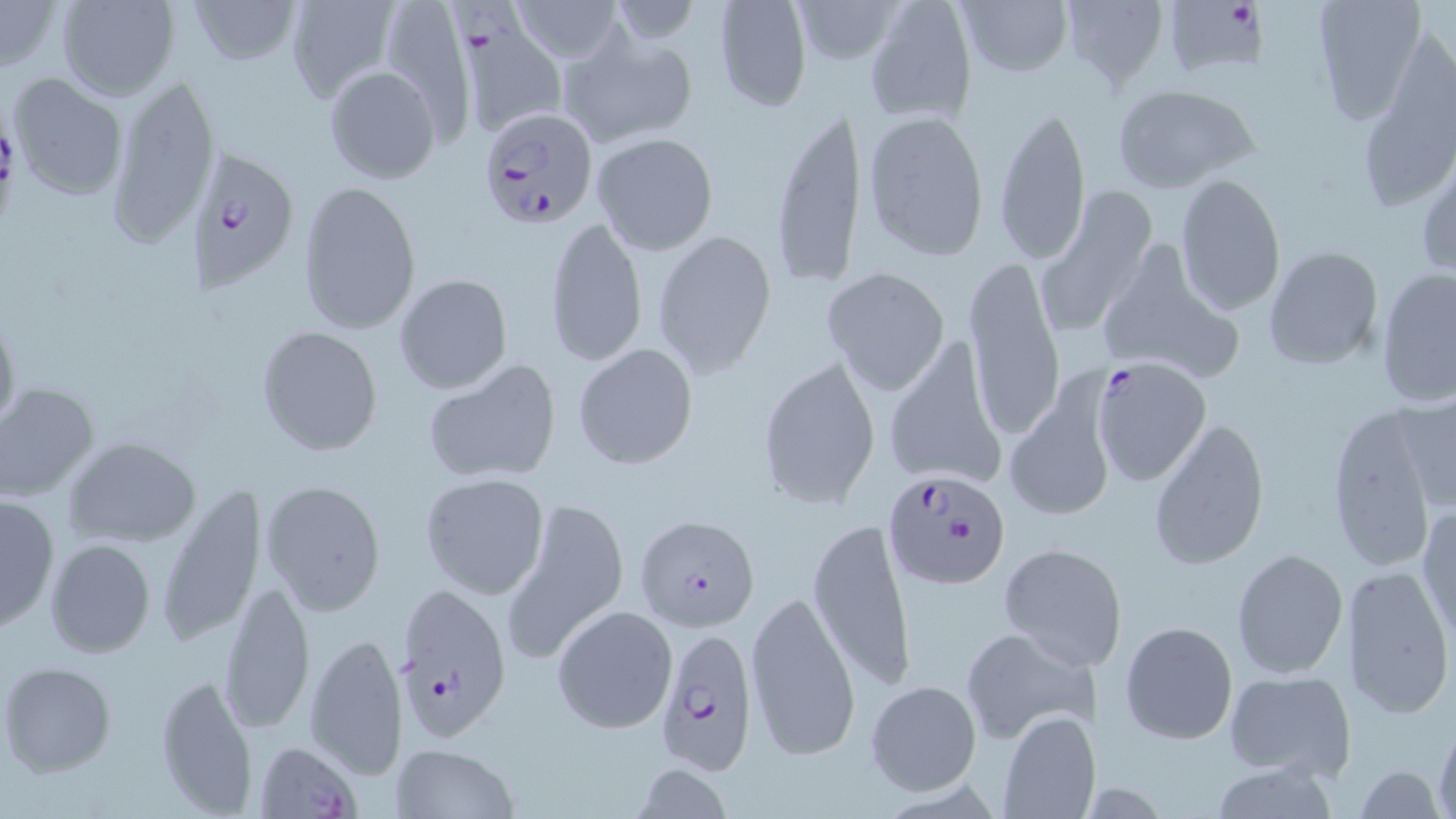

slide_level_diagnosis: Plasmodium falciparum
magnification: 1000x
uninfected_red_blood_cell_locations: 'approximate bounding boxes as (x1,y1)-(x2,y2) corner pairs in pixels: (0,0)-(60,73), (58,0)-(181,102), (184,0)-(304,69), (792,0)-(903,67), (864,0)-(978,125), (954,0)-(1075,79), (1055,0)-(1172,92), (1310,0)-(1428,121), (285,1)-(399,103), (514,1)-(621,62), (712,1)-(813,112), (557,25)-(697,147), (324,63)-(443,184), (6,73)-(128,202), (105,73)-(222,247), (1113,84)-(1258,192), (994,101)-(1091,269), (770,105)-(865,291), (863,108)-(990,262), (591,132)-(719,256), (1417,157)-(1455,279), (1173,173)-(1287,317), (298,180)-(421,335), (1039,183)-(1159,331), (543,214)-(646,370), (652,228)-(777,375), (1095,242)-(1242,381), (1264,245)-(1384,370), (961,255)-(1065,436), (1375,266)-(1455,409), (823,267)-(951,396), (393,273)-(513,394), (0,305)-(20,439), (257,325)-(384,455), (572,345)-(699,469), (881,346)-(1007,490), (756,354)-(881,509), (423,357)-(563,486), (0,382)-(100,502), (1005,382)-(1117,522), (1392,390)-(1456,514), (1325,401)-(1440,573), (1148,417)-(1270,569), (64,436)-(202,548), (419,472)-(550,599), (261,479)-(387,617), (154,483)-(267,647), (502,490)-(632,665), (0,493)-(60,634), (1417,504)-(1455,640), (808,515)-(917,692), (44,538)-(155,658), (998,541)-(1125,669), (1231,547)-(1349,679), (1343,564)-(1454,718), (218,578)-(314,737), (742,585)-(862,764), (552,605)-(678,734), (1118,619)-(1238,746), (958,624)-(1093,745), (303,631)-(408,779), (1,661)-(119,777), (1224,670)-(1355,782), (154,671)-(258,816), (864,679)-(981,795), (997,710)-(1098,819), (1431,720)-(1456,816), (389,744)-(521,819), (1206,762)-(1344,818), (1355,763)-(1445,819)'
stain: May-Grünwald-Giemsa
modality: light microscopy
plasmodium_falciparum_infected_red_blood_cell_locations: 'approximate bounding boxes as (x1,y1)-(x2,y2) corner pairs in pixels: (443,0)-(568,137), (1162,0)-(1267,83), (477,106)-(597,230), (189,147)-(299,289), (1093,356)-(1211,491), (883,469)-(1010,590), (638,515)-(766,633), (392,583)-(512,742), (653,627)-(760,772), (251,737)-(363,819)'
field_of_view: one of a larger specimen
image_size: 1456×819 pixels
preparation: thin blood smear